Describe the morphology of the red blood cells.
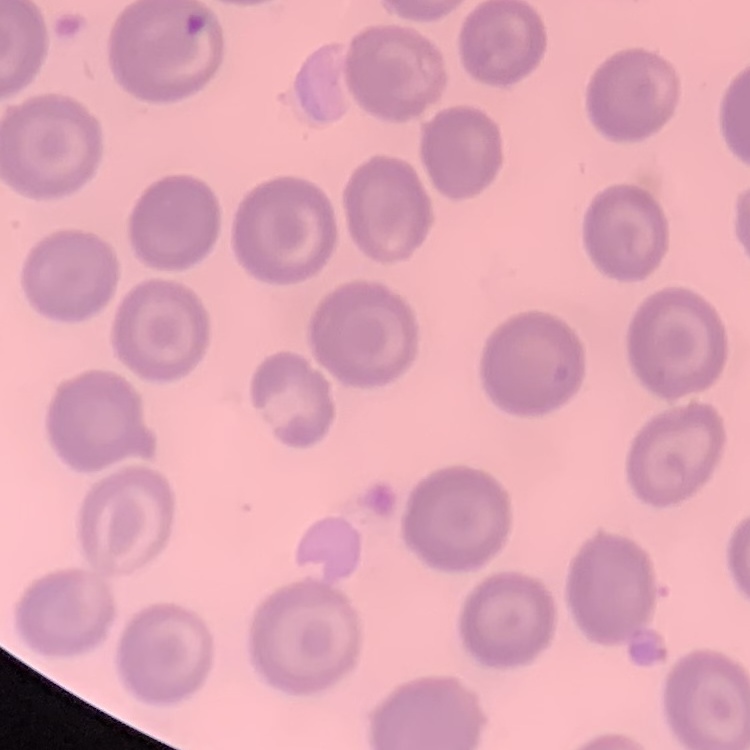
They show no rouleaux formation.

Summary:
  - Image type: one tile cut from a larger photomicrograph
  - Stain: Field's or Giemsa
  - Preparation: thin peripheral smear